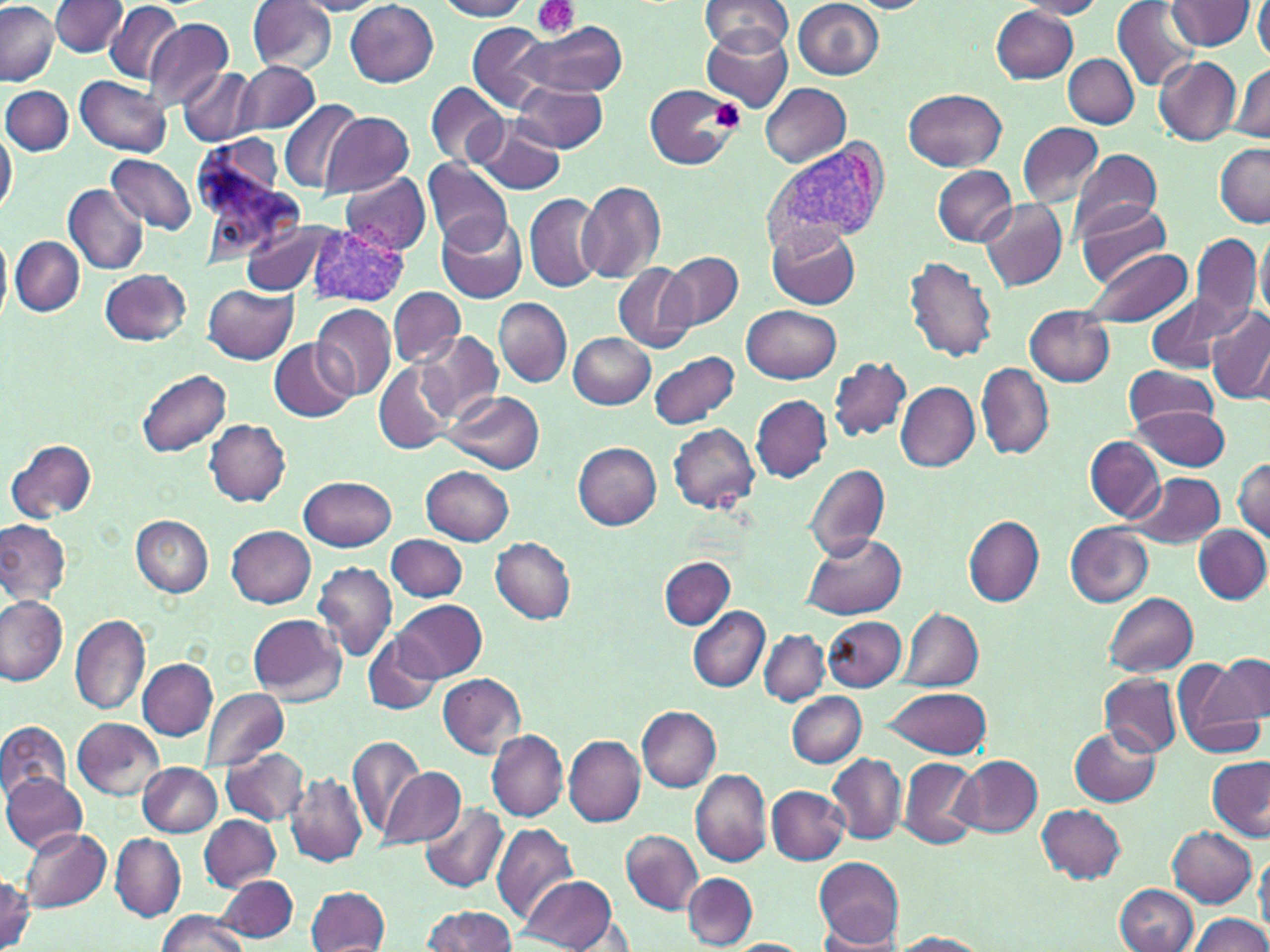

Approximate bounding boxes as (x1, y1, x2, y2) in pixels. Platelet locations: (531, 0, 579, 41), (707, 98, 745, 132). Plasmodium vivax-infected red blood cell locations: (758, 141, 892, 252), (308, 224, 408, 305). Uninfected red blood cell locations: (247, 0, 336, 75), (435, 0, 532, 20), (700, 0, 792, 57), (1015, 0, 1107, 18), (291, 1, 388, 15), (345, 1, 439, 87), (839, 1, 935, 13), (1168, 1, 1258, 51), (1254, 1, 1270, 63), (0, 2, 57, 85), (50, 2, 127, 57), (103, 2, 185, 84), (792, 2, 883, 81), (1112, 2, 1202, 89), (992, 7, 1079, 84), (144, 20, 234, 111), (699, 22, 794, 112), (520, 23, 627, 97), (466, 24, 558, 112), (1064, 53, 1139, 128), (1154, 56, 1241, 146), (234, 61, 321, 135), (1231, 64, 1269, 143), (180, 66, 258, 147), (76, 76, 171, 158), (510, 81, 608, 152), (760, 82, 850, 165), (425, 84, 509, 168), (645, 85, 735, 169), (2, 86, 73, 156), (903, 89, 1007, 171), (919, 91, 1012, 245), (279, 99, 363, 193), (319, 111, 415, 197), (468, 117, 566, 197), (1016, 121, 1104, 207), (0, 126, 17, 221), (1214, 142, 1269, 226), (1070, 148, 1161, 236), (107, 155, 197, 235), (423, 160, 514, 254), (932, 166, 1015, 245), (341, 172, 431, 254), (576, 181, 668, 283), (65, 184, 149, 275), (524, 192, 604, 292), (980, 198, 1069, 294), (1074, 198, 1171, 289), (436, 212, 528, 304), (246, 222, 339, 295), (767, 225, 860, 309), (1255, 229, 1270, 323), (0, 230, 11, 324), (1191, 234, 1260, 330), (12, 237, 84, 316), (1082, 249, 1195, 327), (664, 251, 743, 331), (903, 255, 999, 363), (613, 263, 696, 354), (100, 269, 191, 346), (203, 284, 297, 363), (388, 286, 465, 367), (1146, 294, 1234, 374), (494, 297, 572, 388), (313, 304, 395, 402), (742, 305, 840, 383), (1024, 306, 1115, 387), (1207, 308, 1270, 405), (419, 332, 503, 419), (568, 332, 655, 409), (270, 339, 354, 423), (648, 349, 740, 430), (829, 356, 913, 441), (374, 361, 455, 454), (976, 362, 1054, 460), (1123, 365, 1218, 431), (137, 369, 231, 456), (896, 381, 979, 472), (443, 390, 545, 472), (750, 395, 831, 482), (1129, 404, 1234, 470), (205, 419, 291, 506), (670, 422, 760, 511), (1086, 437, 1164, 522), (7, 438, 97, 524), (571, 442, 662, 529), (1233, 458, 1270, 542), (804, 461, 890, 562), (422, 466, 513, 545), (1125, 472, 1226, 549), (298, 475, 396, 551), (130, 515, 213, 597), (965, 515, 1043, 606), (0, 518, 70, 604), (1065, 523, 1152, 607), (1194, 525, 1270, 604), (227, 526, 317, 608), (802, 532, 907, 620), (386, 534, 466, 601), (491, 537, 576, 623), (660, 557, 735, 629), (313, 561, 398, 662), (1104, 591, 1198, 675), (0, 594, 69, 687), (395, 600, 486, 682), (689, 606, 769, 692), (899, 608, 982, 691), (246, 612, 346, 706), (70, 615, 151, 716), (824, 616, 907, 691), (759, 628, 830, 705), (363, 635, 442, 716), (1173, 655, 1266, 755), (1210, 655, 1268, 725), (138, 659, 217, 740), (436, 673, 526, 759), (1101, 673, 1181, 756), (886, 686, 991, 758), (200, 687, 289, 774), (787, 691, 866, 768), (638, 705, 721, 791), (73, 718, 164, 803), (0, 721, 72, 804), (1070, 726, 1162, 805), (487, 729, 569, 820), (347, 734, 424, 843), (565, 736, 646, 826), (220, 746, 310, 826), (827, 752, 908, 846), (898, 756, 979, 849), (954, 756, 1042, 838), (1207, 756, 1270, 842), (139, 761, 221, 837), (377, 765, 467, 847), (692, 770, 771, 865), (1, 772, 87, 854), (288, 773, 367, 866), (767, 786, 849, 866), (1036, 803, 1126, 885), (421, 805, 508, 892), (201, 815, 281, 890), (492, 821, 577, 924), (1168, 826, 1257, 906), (20, 828, 112, 913), (621, 830, 701, 914), (111, 834, 184, 921), (1256, 849, 1270, 937), (813, 858, 905, 947), (682, 873, 757, 946), (0, 874, 34, 951), (216, 875, 298, 942), (520, 875, 619, 951), (1116, 883, 1198, 952), (306, 885, 390, 952), (423, 905, 517, 952), (156, 912, 251, 952), (1190, 914, 1268, 952), (815, 931, 906, 950), (892, 932, 990, 952), (724, 940, 812, 952). Slide-level diagnosis: Plasmodium vivax. Optical microscopy. Thin blood film. May-Grünwald-Giemsa stain. Single field of view. 1000x magnification. Image is 1270×952 pixels.